Assess the morphology of the erythrocytes.
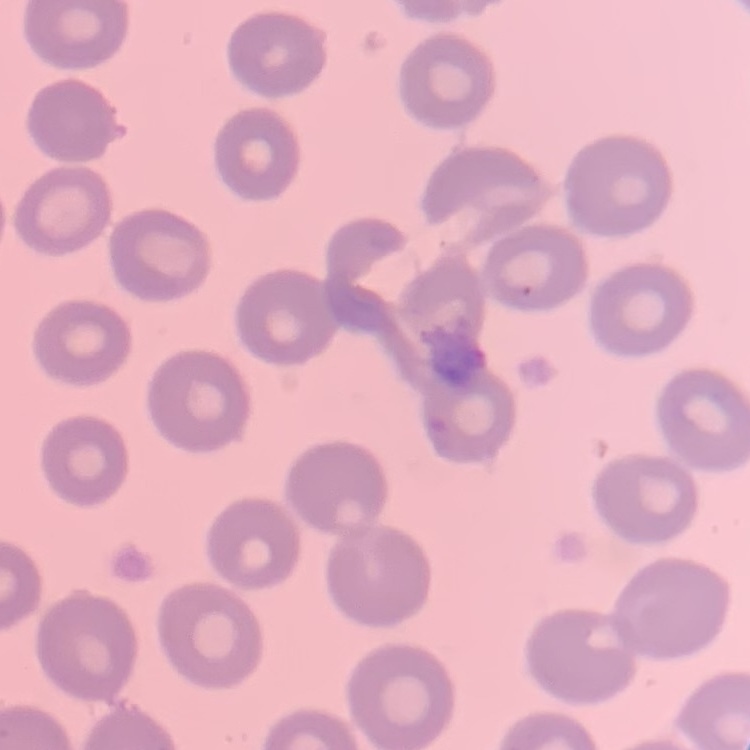

No rouleaux formation.

preparation: thin blood smear
stain: Field's or Giemsa
image_type: one tile cut from a larger photomicrograph